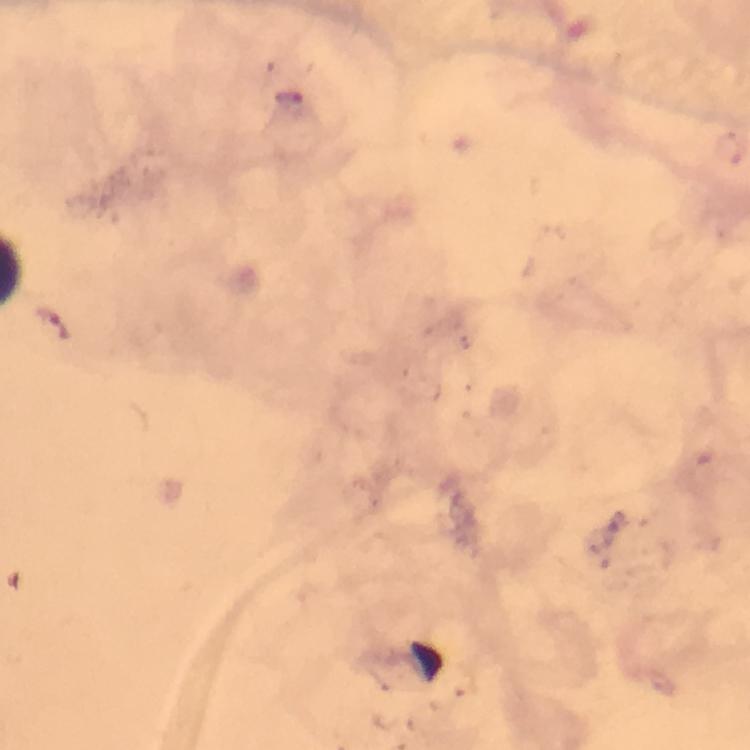

Approximate object centers, in pixels from the top-left corner. Malaria parasite locations: (x=291, y=98). Cropped region of a single field of view. Image is 750×750 pixels. From a malaria diagnostic workup. At 100x magnification. Giemsa-stained preparation. Immersion oil applied. Thick blood film. Photographed with a smartphone mounted on the microscope.